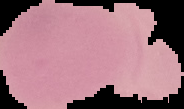
Summary:
  - Result: negative for malaria parasites
  - Image size: 184×109 pixels
  - Image type: segmented cell region with the area outside set to black
  - Preparation: thin blood film